Outline each Plasmodium vivax-infected red blood cell.
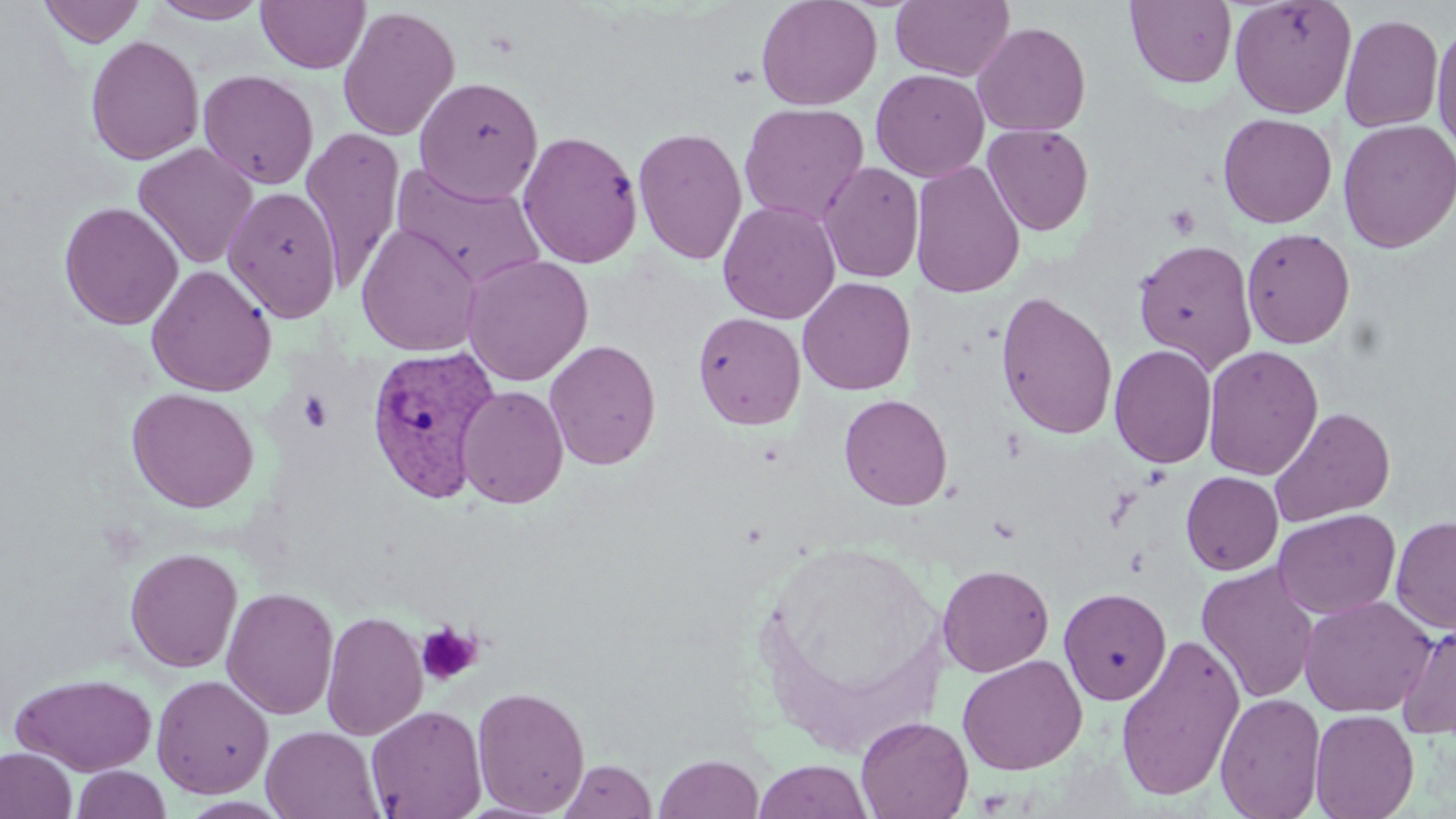
Approximate bounding boxes as (x1,y1)-(x2,y2) corner pairs in pixels.
Plasmodium vivax-infected red blood cells: (365,345)-(502,505).

Summary:
  - Platelet locations: (1165,203)-(1201,240), (296,391)-(334,433), (416,622)-(483,686)
  - Uninfected red blood cell locations: (38,0)-(146,47), (256,0)-(370,73), (756,0)-(882,111), (1125,0)-(1238,89), (1229,0)-(1357,119), (148,1)-(270,24), (890,1)-(1015,82), (338,5)-(460,142), (1340,13)-(1444,133), (1431,19)-(1456,158), (972,21)-(1091,137), (85,35)-(204,165), (870,68)-(989,182), (198,69)-(319,190), (414,76)-(544,204), (738,102)-(869,226), (1229,112)-(1343,348), (1218,113)-(1337,228), (1337,119)-(1456,253), (982,123)-(1095,236), (633,126)-(748,266), (301,128)-(405,290), (517,129)-(643,268), (133,143)-(258,269), (909,160)-(1026,300), (818,161)-(924,283), (391,162)-(546,290), (222,186)-(342,323), (718,200)-(840,324), (58,201)-(183,330), (355,222)-(482,356), (1241,228)-(1355,349), (1133,239)-(1258,372), (461,254)-(594,386), (146,265)-(276,397), (797,276)-(916,395), (995,291)-(1119,440), (692,311)-(806,430), (544,339)-(662,471), (1108,343)-(1218,469), (1202,345)-(1324,480), (456,385)-(569,509), (126,387)-(259,512), (839,393)-(953,510), (1269,407)-(1396,528), (1180,471)-(1283,575), (1272,509)-(1401,619), (1390,515)-(1456,634), (125,547)-(242,673), (1196,562)-(1321,704), (937,564)-(1054,677), (221,586)-(339,720), (1058,587)-(1172,705), (1298,595)-(1437,717), (321,609)-(428,741), (1396,620)-(1456,740), (1115,632)-(1245,801), (957,654)-(1087,775), (11,673)-(158,776), (151,674)-(274,798), (472,685)-(591,817), (1215,692)-(1326,819), (366,704)-(487,819), (1309,708)-(1419,819), (856,715)-(974,818), (261,726)-(383,819), (0,746)-(77,819), (654,753)-(765,819), (560,760)-(657,818), (753,760)-(873,818), (71,765)-(172,819)
  - Slide-level diagnosis: Plasmodium vivax
  - Magnification: 1000x
  - Stain: May-Grünwald-Giemsa
  - Image size: 1456×819 pixels
  - Preparation: thin blood film
  - Field of view: one of a larger specimen
  - Modality: light microscopy